Assess this cell for malaria.
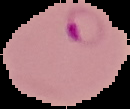
It is parasitized.

The area outside the segmented cell region is set to black. From a thin blood smear. Image is 130×109 pixels.